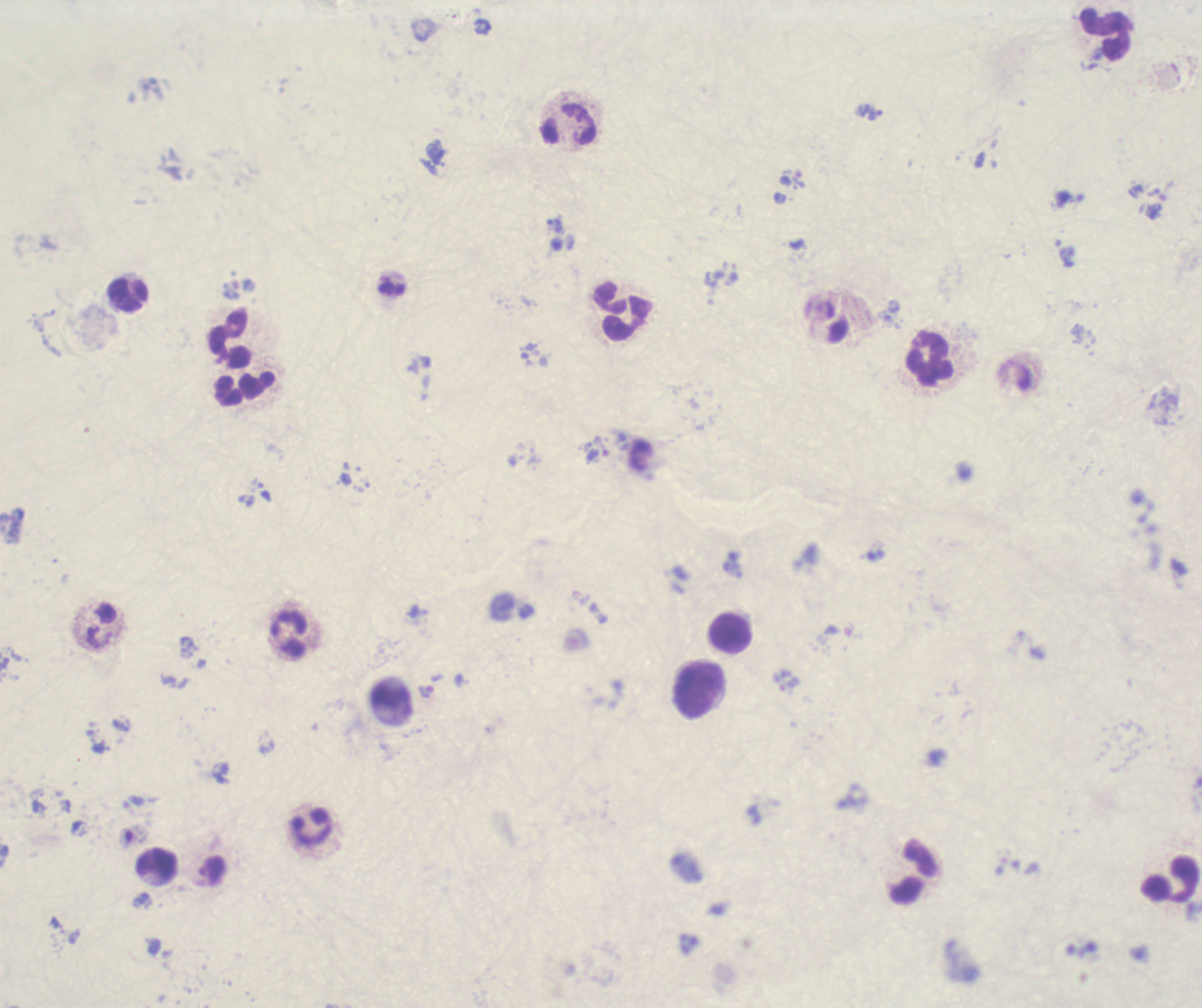

Approximate centers as {x, y} in pixels. Trophozoite locations: {869, 112}. Leukocyte locations: {1105, 34}, {128, 295}, {621, 312}, {229, 340}, {930, 359}, {246, 388}, {730, 634}, {289, 635}, {697, 688}, {158, 865}, {915, 874}, {1170, 880}. Image is 1202×1008 pixels. Background quality: poor. 100x magnification. Single field of view. Previously used in an actual diagnosis. Thick smear of blood. Romanowsky stain. Result: positive for Plasmodium parasites.